Classify this cell by malaria status.
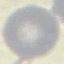

Uninfected.

image type = automatically extracted cell patch, resized to 64 × 64 pixels
preparation = thin smear
stain = Giemsa
capture = smartphone camera at the microscope eyepiece